Locate and identify every blood parasite.
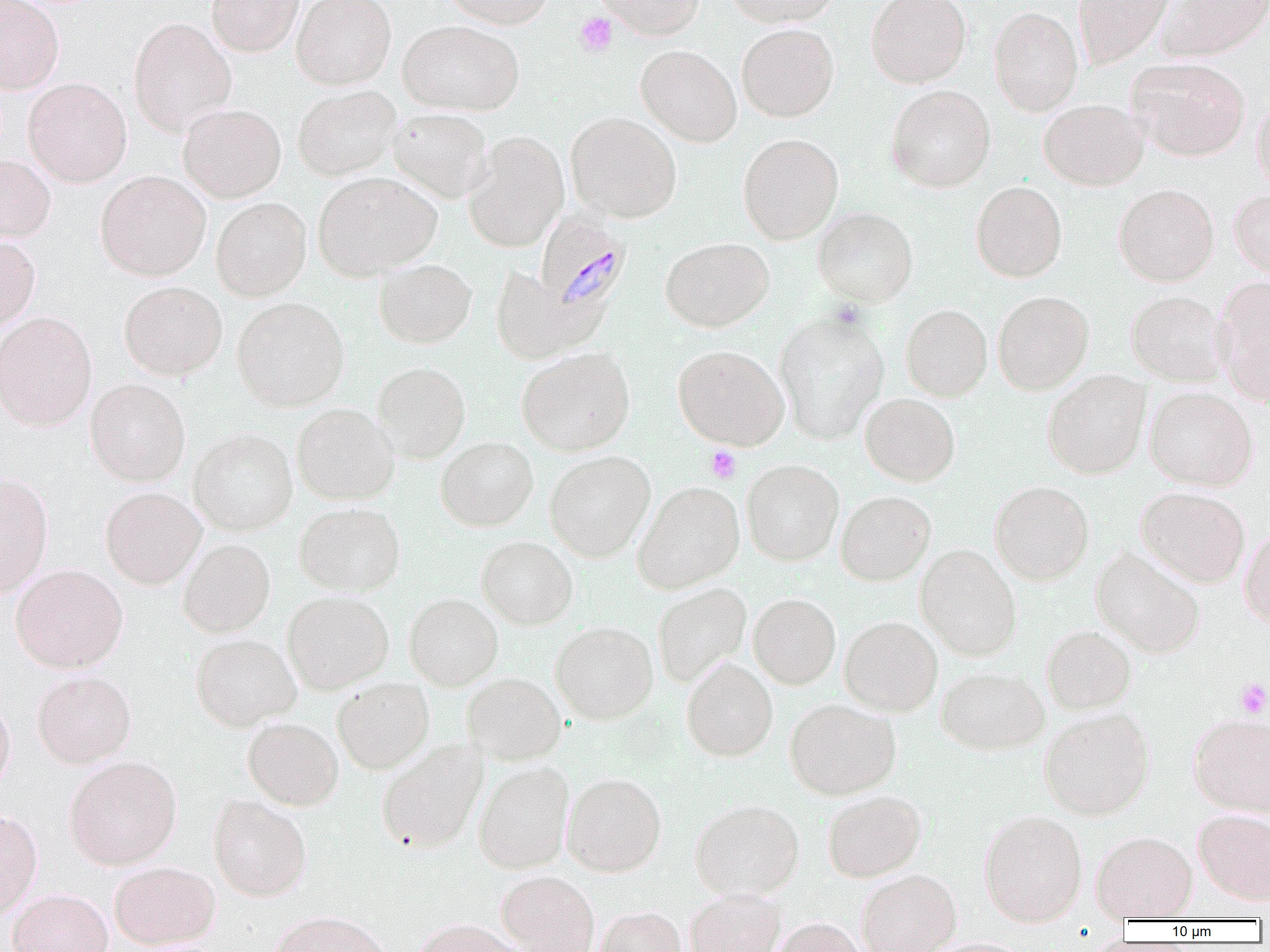

Approximate bounding boxes as named x1/y1/x2/y2 corners in pixels.
Plasmodium malariae-infected red blood cells: (x1=535, y1=210, x2=633, y2=317).
No Plasmodium falciparum, Plasmodium ovale, Plasmodium vivax, Babesia divergens, or Trypanosoma brucei observed.

Summary:
  - Uninfected red blood cell locations: (x1=0, y1=0, x2=64, y2=93), (x1=206, y1=0, x2=303, y2=57), (x1=292, y1=0, x2=396, y2=89), (x1=441, y1=0, x2=555, y2=28), (x1=594, y1=0, x2=705, y2=39), (x1=726, y1=0, x2=843, y2=26), (x1=866, y1=0, x2=971, y2=87), (x1=1073, y1=0, x2=1174, y2=68), (x1=1157, y1=0, x2=1270, y2=61), (x1=989, y1=6, x2=1083, y2=116), (x1=129, y1=17, x2=236, y2=136), (x1=398, y1=19, x2=523, y2=115), (x1=737, y1=23, x2=839, y2=122), (x1=636, y1=45, x2=741, y2=146), (x1=1126, y1=57, x2=1251, y2=161), (x1=23, y1=77, x2=132, y2=187), (x1=293, y1=84, x2=401, y2=180), (x1=886, y1=85, x2=996, y2=193), (x1=1251, y1=94, x2=1270, y2=196), (x1=1038, y1=99, x2=1148, y2=190), (x1=181, y1=100, x2=402, y2=192), (x1=178, y1=104, x2=286, y2=203), (x1=389, y1=107, x2=493, y2=202), (x1=565, y1=112, x2=682, y2=222), (x1=463, y1=131, x2=569, y2=252), (x1=737, y1=133, x2=843, y2=245), (x1=0, y1=154, x2=55, y2=243), (x1=95, y1=170, x2=211, y2=281), (x1=313, y1=172, x2=441, y2=280), (x1=971, y1=181, x2=1067, y2=282), (x1=1114, y1=184, x2=1219, y2=286), (x1=1229, y1=189, x2=1270, y2=283), (x1=211, y1=197, x2=312, y2=301), (x1=812, y1=207, x2=919, y2=307), (x1=0, y1=235, x2=40, y2=331), (x1=660, y1=237, x2=774, y2=332), (x1=374, y1=258, x2=476, y2=348), (x1=490, y1=267, x2=603, y2=363), (x1=1213, y1=276, x2=1270, y2=405), (x1=119, y1=281, x2=227, y2=379), (x1=992, y1=290, x2=1093, y2=395), (x1=1126, y1=290, x2=1231, y2=386), (x1=231, y1=297, x2=349, y2=412), (x1=901, y1=304, x2=992, y2=400), (x1=0, y1=311, x2=97, y2=430), (x1=774, y1=311, x2=889, y2=444), (x1=673, y1=345, x2=789, y2=450), (x1=517, y1=347, x2=635, y2=455), (x1=372, y1=362, x2=471, y2=463), (x1=1042, y1=370, x2=1150, y2=479), (x1=85, y1=378, x2=190, y2=486), (x1=1144, y1=386, x2=1258, y2=491), (x1=860, y1=393, x2=960, y2=486), (x1=292, y1=403, x2=399, y2=505), (x1=189, y1=427, x2=297, y2=535), (x1=435, y1=437, x2=538, y2=531), (x1=544, y1=450, x2=655, y2=562), (x1=742, y1=459, x2=844, y2=565), (x1=0, y1=474, x2=53, y2=596), (x1=990, y1=480, x2=1094, y2=585), (x1=633, y1=481, x2=745, y2=592), (x1=1135, y1=486, x2=1250, y2=587), (x1=100, y1=487, x2=206, y2=589), (x1=836, y1=491, x2=936, y2=586), (x1=294, y1=502, x2=405, y2=595), (x1=1239, y1=525, x2=1270, y2=630), (x1=476, y1=535, x2=578, y2=629), (x1=178, y1=538, x2=275, y2=637), (x1=915, y1=544, x2=1023, y2=660), (x1=1091, y1=546, x2=1206, y2=658), (x1=10, y1=564, x2=128, y2=673), (x1=652, y1=582, x2=751, y2=688), (x1=282, y1=590, x2=394, y2=694), (x1=404, y1=592, x2=503, y2=690), (x1=749, y1=593, x2=841, y2=689), (x1=839, y1=615, x2=943, y2=716), (x1=550, y1=620, x2=658, y2=724), (x1=1042, y1=625, x2=1136, y2=714), (x1=190, y1=633, x2=301, y2=731), (x1=681, y1=657, x2=778, y2=761), (x1=936, y1=666, x2=1050, y2=754), (x1=31, y1=670, x2=137, y2=768), (x1=462, y1=672, x2=567, y2=764), (x1=333, y1=677, x2=435, y2=774), (x1=0, y1=696, x2=15, y2=795), (x1=785, y1=698, x2=901, y2=799), (x1=1038, y1=707, x2=1155, y2=820), (x1=1189, y1=713, x2=1270, y2=816), (x1=243, y1=717, x2=343, y2=810), (x1=376, y1=738, x2=488, y2=852), (x1=64, y1=755, x2=182, y2=870), (x1=473, y1=760, x2=574, y2=873), (x1=562, y1=772, x2=667, y2=876), (x1=821, y1=790, x2=926, y2=881), (x1=208, y1=794, x2=312, y2=901), (x1=690, y1=798, x2=805, y2=900), (x1=978, y1=809, x2=1087, y2=927), (x1=1193, y1=809, x2=1270, y2=905), (x1=0, y1=810, x2=43, y2=920), (x1=1091, y1=830, x2=1198, y2=921), (x1=109, y1=860, x2=221, y2=950), (x1=856, y1=869, x2=961, y2=952), (x1=496, y1=870, x2=600, y2=952), (x1=8, y1=888, x2=113, y2=952), (x1=684, y1=888, x2=786, y2=952), (x1=593, y1=906, x2=688, y2=952), (x1=268, y1=910, x2=393, y2=952), (x1=768, y1=917, x2=870, y2=952), (x1=412, y1=918, x2=526, y2=952)
  - Platelet locations: (x1=575, y1=12, x2=618, y2=57), (x1=705, y1=445, x2=741, y2=483), (x1=1234, y1=678, x2=1270, y2=718)
  - Slide-level diagnosis: Plasmodium malariae
  - Modality: optical microscopy
  - Magnification: 1000x
  - Preparation: thin blood film
  - Image size: 1270×952 pixels
  - Field of view: single